Assess the morphology of the red blood cells.
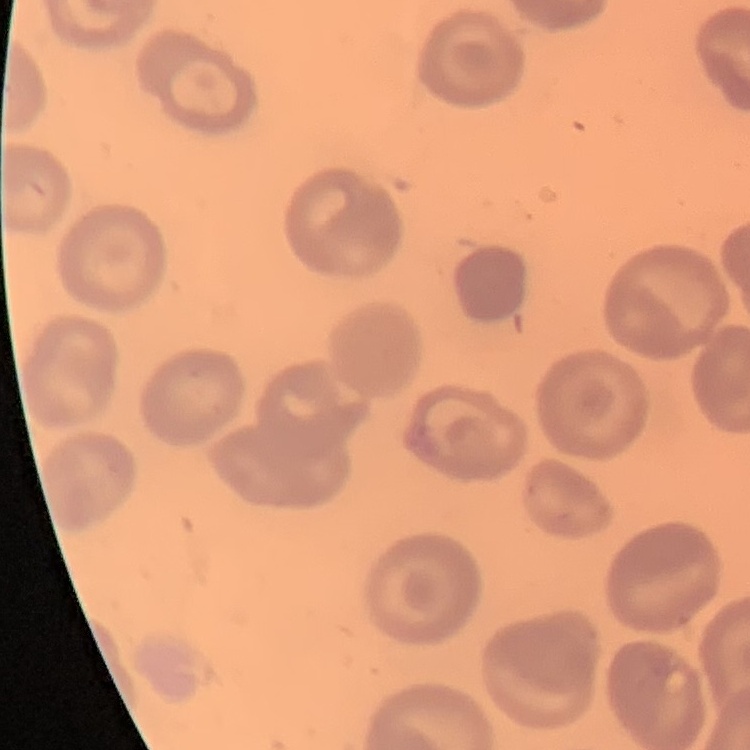

No rouleaux formation.

Summary:
  - Image type: square crop of a larger photomicrograph
  - Preparation: thin blood smear
  - Stain: Field's or Giemsa